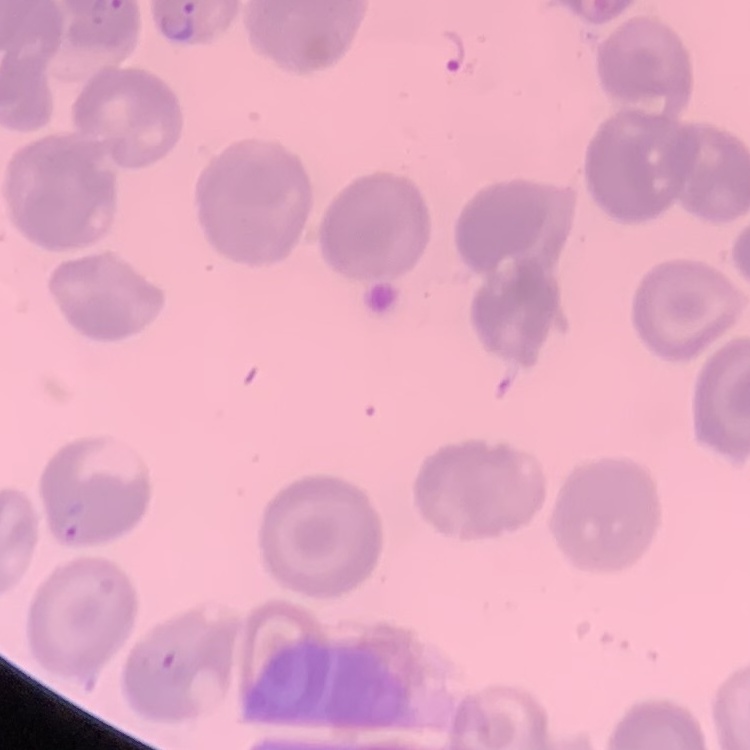 The red blood cells show no rouleaux formation. One tile cut from a larger photomicrograph. Stained with either Field's or Giemsa. Thin blood film.